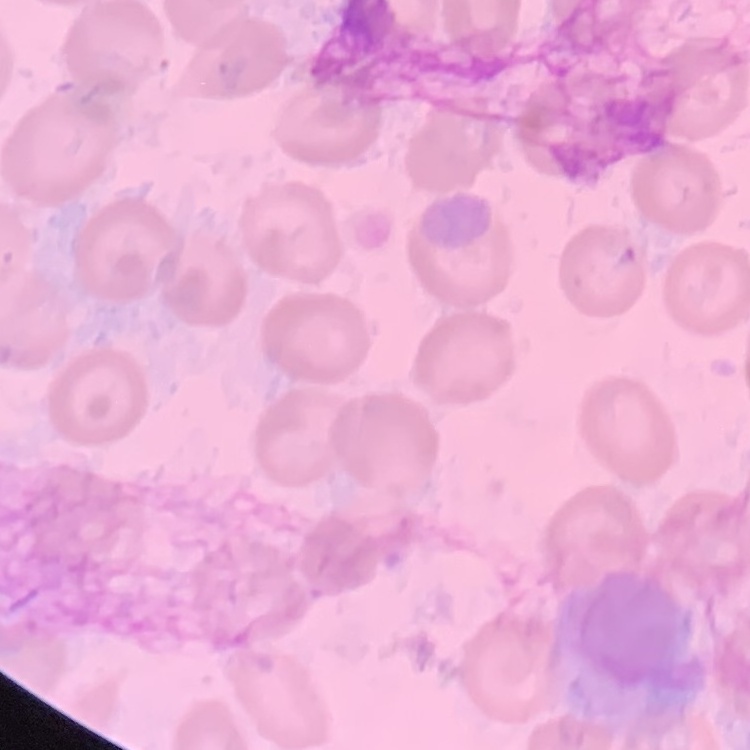

The erythrocytes exhibit no rouleaux formation. Field's or Giemsa stain. Thin peripheral smear. One tile cut from a larger photomicrograph.